Outline each blood parasite and name the species.
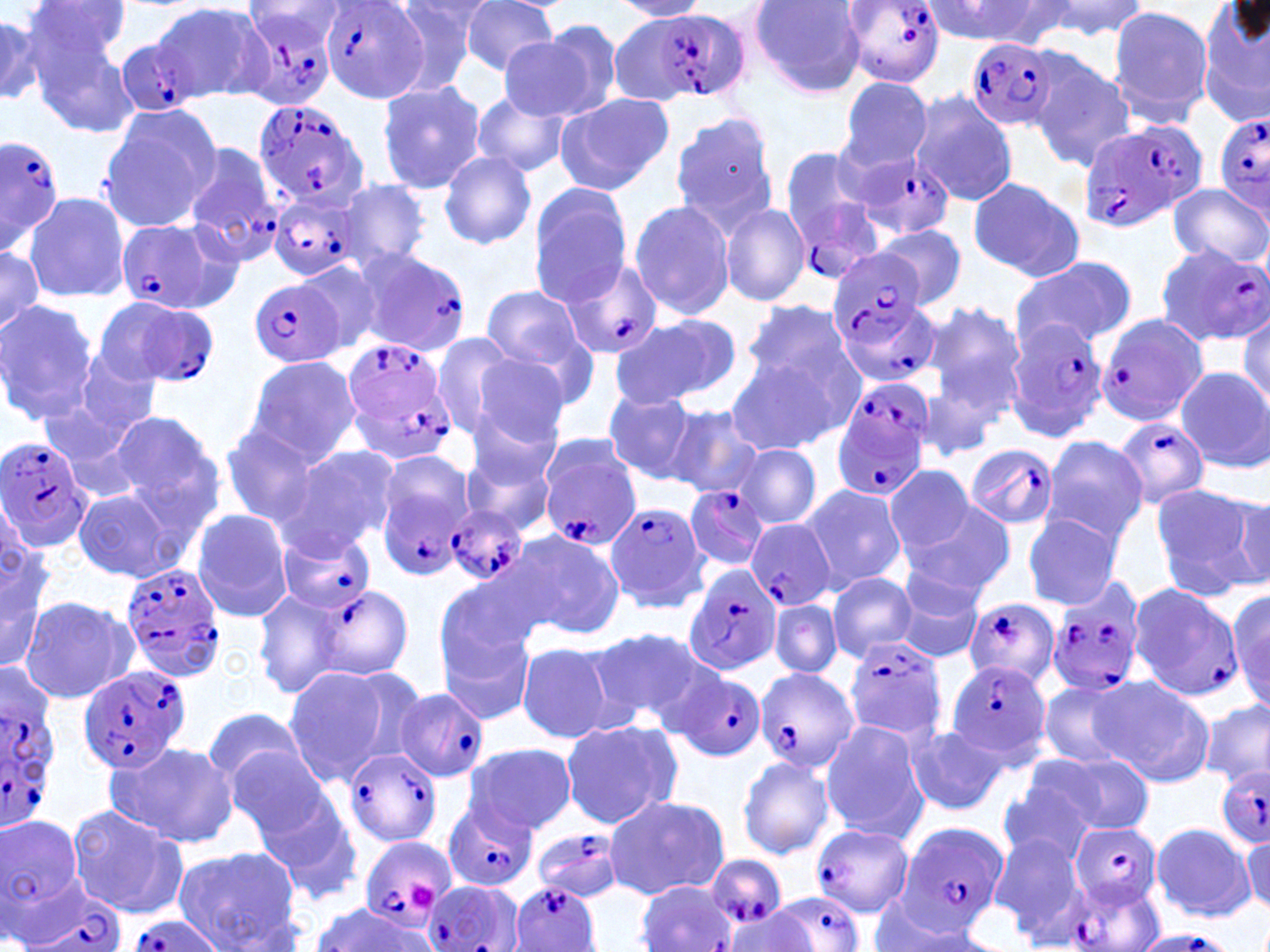
Approximate bounding boxes as named x1/y1/x2/y2 corners in pixels.
Plasmodium falciparum-infected red blood cells: (x1=841, y1=0, x2=946, y2=86), (x1=320, y1=2, x2=428, y2=104), (x1=240, y1=4, x2=342, y2=110), (x1=618, y1=9, x2=750, y2=103), (x1=116, y1=37, x2=205, y2=116), (x1=967, y1=37, x2=1058, y2=132), (x1=252, y1=98, x2=369, y2=210), (x1=1214, y1=113, x2=1270, y2=216), (x1=1077, y1=119, x2=1205, y2=236), (x1=0, y1=134, x2=69, y2=255), (x1=181, y1=142, x2=285, y2=266), (x1=779, y1=147, x2=887, y2=275), (x1=848, y1=150, x2=956, y2=238), (x1=266, y1=191, x2=361, y2=283), (x1=116, y1=215, x2=242, y2=314), (x1=1155, y1=242, x2=1270, y2=345), (x1=357, y1=249, x2=471, y2=357), (x1=831, y1=249, x2=929, y2=344), (x1=560, y1=259, x2=662, y2=361), (x1=251, y1=278, x2=344, y2=369), (x1=833, y1=294, x2=941, y2=391), (x1=104, y1=297, x2=220, y2=389), (x1=1095, y1=313, x2=1209, y2=428), (x1=1005, y1=318, x2=1109, y2=444), (x1=342, y1=338, x2=455, y2=463), (x1=830, y1=384, x2=934, y2=498), (x1=1115, y1=416, x2=1210, y2=509), (x1=0, y1=437, x2=92, y2=555), (x1=965, y1=444, x2=1058, y2=528), (x1=541, y1=451, x2=642, y2=552), (x1=684, y1=484, x2=769, y2=569), (x1=378, y1=488, x2=468, y2=582), (x1=605, y1=501, x2=709, y2=614), (x1=446, y1=505, x2=529, y2=587), (x1=747, y1=520, x2=836, y2=612), (x1=276, y1=530, x2=376, y2=615), (x1=120, y1=560, x2=227, y2=684), (x1=683, y1=564, x2=783, y2=677), (x1=1047, y1=576, x2=1146, y2=697), (x1=1128, y1=582, x2=1242, y2=701), (x1=311, y1=585, x2=413, y2=679), (x1=964, y1=598, x2=1058, y2=691), (x1=844, y1=637, x2=949, y2=744), (x1=944, y1=658, x2=1048, y2=762), (x1=77, y1=665, x2=190, y2=776), (x1=755, y1=667, x2=859, y2=775), (x1=670, y1=668, x2=765, y2=762), (x1=0, y1=675, x2=63, y2=828), (x1=395, y1=687, x2=488, y2=782), (x1=344, y1=748, x2=442, y2=847), (x1=1216, y1=764, x2=1270, y2=847), (x1=442, y1=798, x2=537, y2=893), (x1=895, y1=822, x2=1008, y2=933), (x1=1071, y1=823, x2=1163, y2=908), (x1=812, y1=824, x2=914, y2=917), (x1=532, y1=828, x2=623, y2=903), (x1=360, y1=837, x2=454, y2=931), (x1=705, y1=854, x2=787, y2=933), (x1=17, y1=878, x2=126, y2=952), (x1=1059, y1=878, x2=1162, y2=952), (x1=422, y1=879, x2=517, y2=952), (x1=636, y1=879, x2=736, y2=952), (x1=510, y1=880, x2=600, y2=952), (x1=769, y1=890, x2=865, y2=952), (x1=125, y1=915, x2=225, y2=952), (x1=1129, y1=931, x2=1239, y2=952).
No Plasmodium ovale, Plasmodium malariae, Plasmodium vivax, Babesia divergens, or Trypanosoma brucei observed.

slide_level_diagnosis: Plasmodium falciparum
uninfected_red_blood_cell_locations: 'approximate bounding boxes as named x1/y1/x2/y2 corners in pixels: (x1=383, y1=0, x2=486, y2=96), (x1=457, y1=0, x2=560, y2=76), (x1=613, y1=0, x2=711, y2=20), (x1=748, y1=0, x2=869, y2=97), (x1=930, y1=0, x2=1067, y2=46), (x1=1038, y1=0, x2=1150, y2=39), (x1=27, y1=1, x2=133, y2=66), (x1=152, y1=2, x2=270, y2=103), (x1=1198, y1=3, x2=1270, y2=127), (x1=0, y1=4, x2=86, y2=106), (x1=1106, y1=6, x2=1214, y2=126), (x1=0, y1=13, x2=43, y2=105), (x1=25, y1=22, x2=140, y2=136), (x1=500, y1=27, x2=617, y2=123), (x1=1027, y1=54, x2=1136, y2=171), (x1=838, y1=77, x2=933, y2=172), (x1=376, y1=80, x2=488, y2=195), (x1=469, y1=90, x2=570, y2=178), (x1=907, y1=91, x2=1020, y2=207), (x1=554, y1=94, x2=672, y2=195), (x1=99, y1=107, x2=221, y2=232), (x1=669, y1=111, x2=780, y2=237), (x1=437, y1=151, x2=537, y2=249), (x1=965, y1=176, x2=1084, y2=283), (x1=339, y1=179, x2=433, y2=271), (x1=527, y1=183, x2=633, y2=304), (x1=1166, y1=183, x2=1269, y2=270), (x1=23, y1=192, x2=131, y2=303), (x1=629, y1=199, x2=735, y2=321), (x1=719, y1=202, x2=809, y2=307), (x1=875, y1=225, x2=966, y2=310), (x1=0, y1=242, x2=44, y2=339), (x1=1012, y1=252, x2=1137, y2=350), (x1=296, y1=259, x2=384, y2=354), (x1=479, y1=285, x2=592, y2=386), (x1=742, y1=299, x2=857, y2=397), (x1=0, y1=300, x2=98, y2=426), (x1=921, y1=301, x2=1024, y2=421), (x1=1237, y1=310, x2=1269, y2=408), (x1=612, y1=313, x2=740, y2=407), (x1=433, y1=331, x2=524, y2=436), (x1=463, y1=348, x2=576, y2=454), (x1=72, y1=351, x2=161, y2=435), (x1=722, y1=354, x2=844, y2=457), (x1=244, y1=355, x2=361, y2=463), (x1=1176, y1=367, x2=1269, y2=471), (x1=602, y1=391, x2=703, y2=484), (x1=42, y1=401, x2=151, y2=504), (x1=463, y1=403, x2=563, y2=506), (x1=663, y1=406, x2=762, y2=499), (x1=105, y1=409, x2=223, y2=520), (x1=220, y1=421, x2=329, y2=526), (x1=1040, y1=436, x2=1147, y2=546), (x1=276, y1=444, x2=398, y2=556), (x1=736, y1=444, x2=821, y2=529), (x1=374, y1=448, x2=476, y2=549), (x1=462, y1=448, x2=559, y2=540), (x1=884, y1=465, x2=977, y2=556), (x1=799, y1=483, x2=905, y2=592), (x1=1149, y1=483, x2=1259, y2=596), (x1=72, y1=488, x2=189, y2=582), (x1=1218, y1=491, x2=1270, y2=589), (x1=899, y1=499, x2=1017, y2=598), (x1=191, y1=509, x2=293, y2=621), (x1=1022, y1=513, x2=1123, y2=609), (x1=508, y1=529, x2=625, y2=640), (x1=0, y1=544, x2=51, y2=672), (x1=890, y1=566, x2=986, y2=663), (x1=827, y1=572, x2=920, y2=662), (x1=433, y1=575, x2=540, y2=684), (x1=1223, y1=583, x2=1270, y2=710), (x1=252, y1=588, x2=347, y2=700), (x1=18, y1=595, x2=136, y2=705), (x1=770, y1=600, x2=842, y2=677), (x1=436, y1=620, x2=538, y2=728), (x1=589, y1=627, x2=721, y2=729), (x1=517, y1=643, x2=616, y2=742), (x1=279, y1=663, x2=412, y2=785), (x1=1091, y1=677, x2=1216, y2=787), (x1=1035, y1=679, x2=1140, y2=772), (x1=1202, y1=697, x2=1270, y2=789), (x1=202, y1=708, x2=312, y2=791), (x1=559, y1=717, x2=683, y2=831), (x1=819, y1=720, x2=929, y2=843), (x1=903, y1=723, x2=1009, y2=817), (x1=105, y1=740, x2=238, y2=849), (x1=464, y1=742, x2=577, y2=835), (x1=225, y1=745, x2=339, y2=848), (x1=1026, y1=750, x2=1154, y2=840), (x1=737, y1=755, x2=835, y2=859), (x1=998, y1=769, x2=1106, y2=866), (x1=249, y1=776, x2=362, y2=898), (x1=603, y1=794, x2=732, y2=900), (x1=65, y1=804, x2=190, y2=918), (x1=0, y1=813, x2=86, y2=921), (x1=1150, y1=823, x2=1254, y2=922), (x1=1239, y1=829, x2=1270, y2=918), (x1=989, y1=832, x2=1089, y2=942), (x1=174, y1=846, x2=302, y2=950), (x1=867, y1=899, x2=991, y2=951), (x1=309, y1=902, x2=433, y2=949), (x1=723, y1=907, x2=817, y2=951)'
image_size: 1270×952 pixels
modality: light microscopy
field_of_view: one of a larger specimen
platelet_locations: 'approximate bounding boxes as named x1/y1/x2/y2 corners in pixels: (x1=409, y1=883, x2=441, y2=912)'
stain: May-Grünwald-Giemsa
preparation: thin blood film
magnification: 1000x